Classify this cell by malaria status.
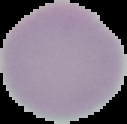
It is uninfected.

Image is 127×124 pixels. From a thin blood smear. Segmented cell region on a black background.